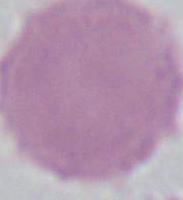
modality = micrograph
identification = red blood cell
magnification = 1000x